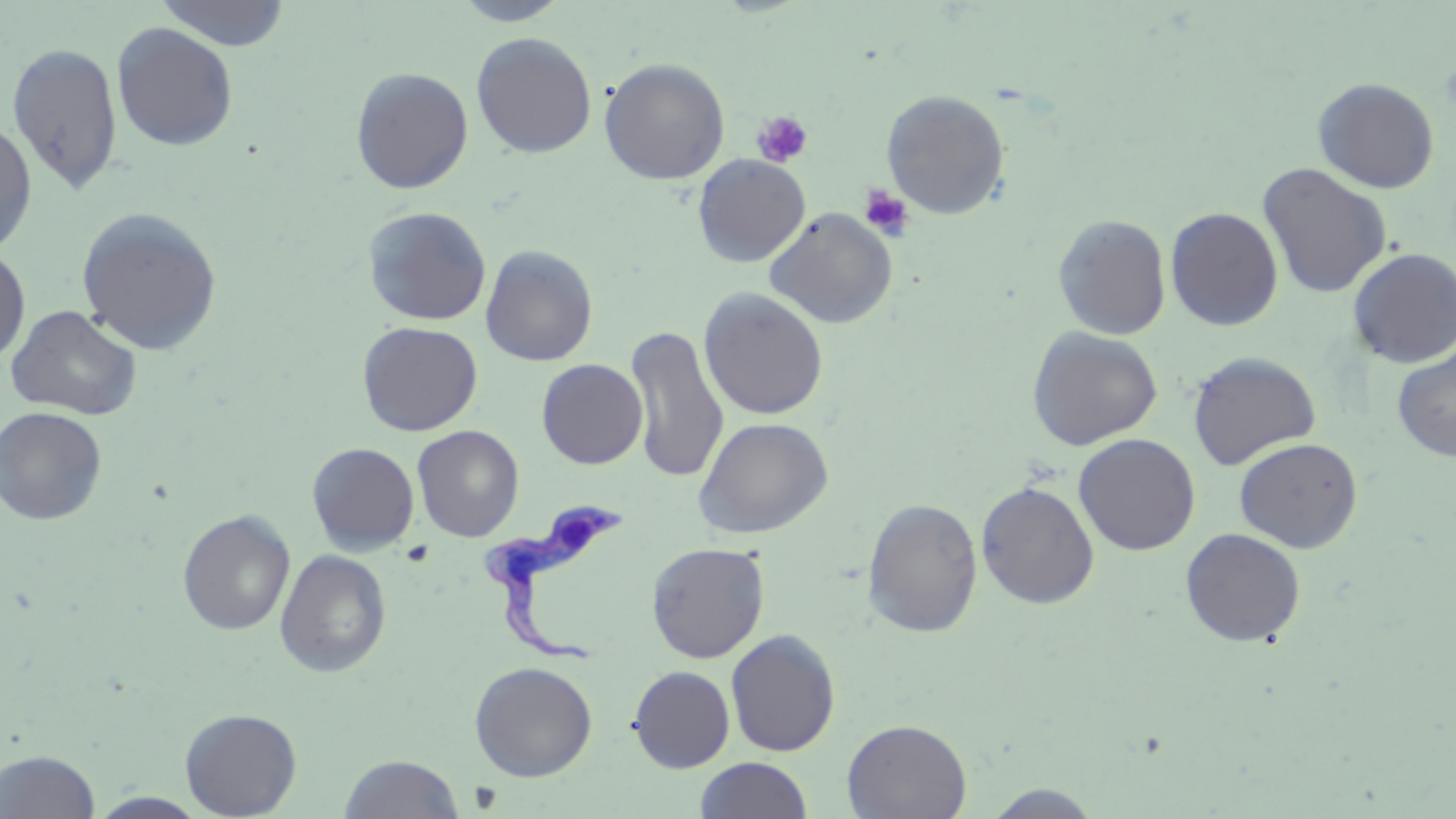

Trypanosoma brucei locations = approximate bounding boxes as named x1/y1/x2/y2 corners in pixels: (x1=474, y1=498, x2=627, y2=669)
slide-level diagnosis = Trypanosoma brucei
platelet locations = approximate bounding boxes as named x1/y1/x2/y2 corners in pixels: (x1=752, y1=110, x2=814, y2=168), (x1=859, y1=184, x2=914, y2=240)
magnification = 1000x
uninfected red blood cell locations = approximate bounding boxes as named x1/y1/x2/y2 corners in pixels: (x1=155, y1=0, x2=292, y2=51), (x1=451, y1=0, x2=572, y2=26), (x1=112, y1=22, x2=239, y2=151), (x1=471, y1=32, x2=597, y2=158), (x1=6, y1=42, x2=124, y2=197), (x1=599, y1=58, x2=730, y2=185), (x1=351, y1=66, x2=474, y2=194), (x1=1313, y1=77, x2=1440, y2=193), (x1=880, y1=89, x2=1010, y2=219), (x1=0, y1=120, x2=37, y2=256), (x1=692, y1=154, x2=810, y2=267), (x1=1257, y1=162, x2=1392, y2=300), (x1=362, y1=206, x2=491, y2=325), (x1=76, y1=207, x2=223, y2=355), (x1=765, y1=207, x2=897, y2=328), (x1=1165, y1=207, x2=1284, y2=331), (x1=1052, y1=214, x2=1172, y2=340), (x1=0, y1=244, x2=31, y2=366), (x1=481, y1=244, x2=598, y2=366), (x1=1347, y1=247, x2=1456, y2=369), (x1=699, y1=288, x2=829, y2=421), (x1=5, y1=305, x2=143, y2=420), (x1=357, y1=321, x2=482, y2=436), (x1=626, y1=324, x2=728, y2=484), (x1=1026, y1=326, x2=1163, y2=450), (x1=1392, y1=344, x2=1456, y2=462), (x1=1187, y1=351, x2=1322, y2=470), (x1=536, y1=359, x2=648, y2=469), (x1=1, y1=406, x2=107, y2=525), (x1=693, y1=416, x2=833, y2=539), (x1=412, y1=425, x2=524, y2=542), (x1=1074, y1=433, x2=1201, y2=556), (x1=1234, y1=437, x2=1364, y2=552), (x1=307, y1=442, x2=419, y2=555), (x1=976, y1=480, x2=1099, y2=609), (x1=862, y1=497, x2=983, y2=637), (x1=177, y1=510, x2=295, y2=635), (x1=1180, y1=528, x2=1306, y2=647), (x1=645, y1=541, x2=769, y2=663), (x1=275, y1=549, x2=392, y2=677), (x1=725, y1=629, x2=840, y2=757), (x1=469, y1=661, x2=598, y2=781), (x1=628, y1=665, x2=735, y2=773), (x1=179, y1=708, x2=302, y2=818), (x1=842, y1=718, x2=972, y2=819), (x1=1, y1=749, x2=101, y2=818), (x1=339, y1=754, x2=465, y2=818), (x1=694, y1=757, x2=813, y2=818), (x1=981, y1=784, x2=1107, y2=817), (x1=87, y1=792, x2=210, y2=818)
preparation = thin blood film
stain = May-Grünwald-Giemsa
field of view = one of a larger specimen
image size = 1456×819 pixels
modality = light microscopy